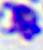

modality = photomicrograph
identification = white blood cell
magnification = 400x